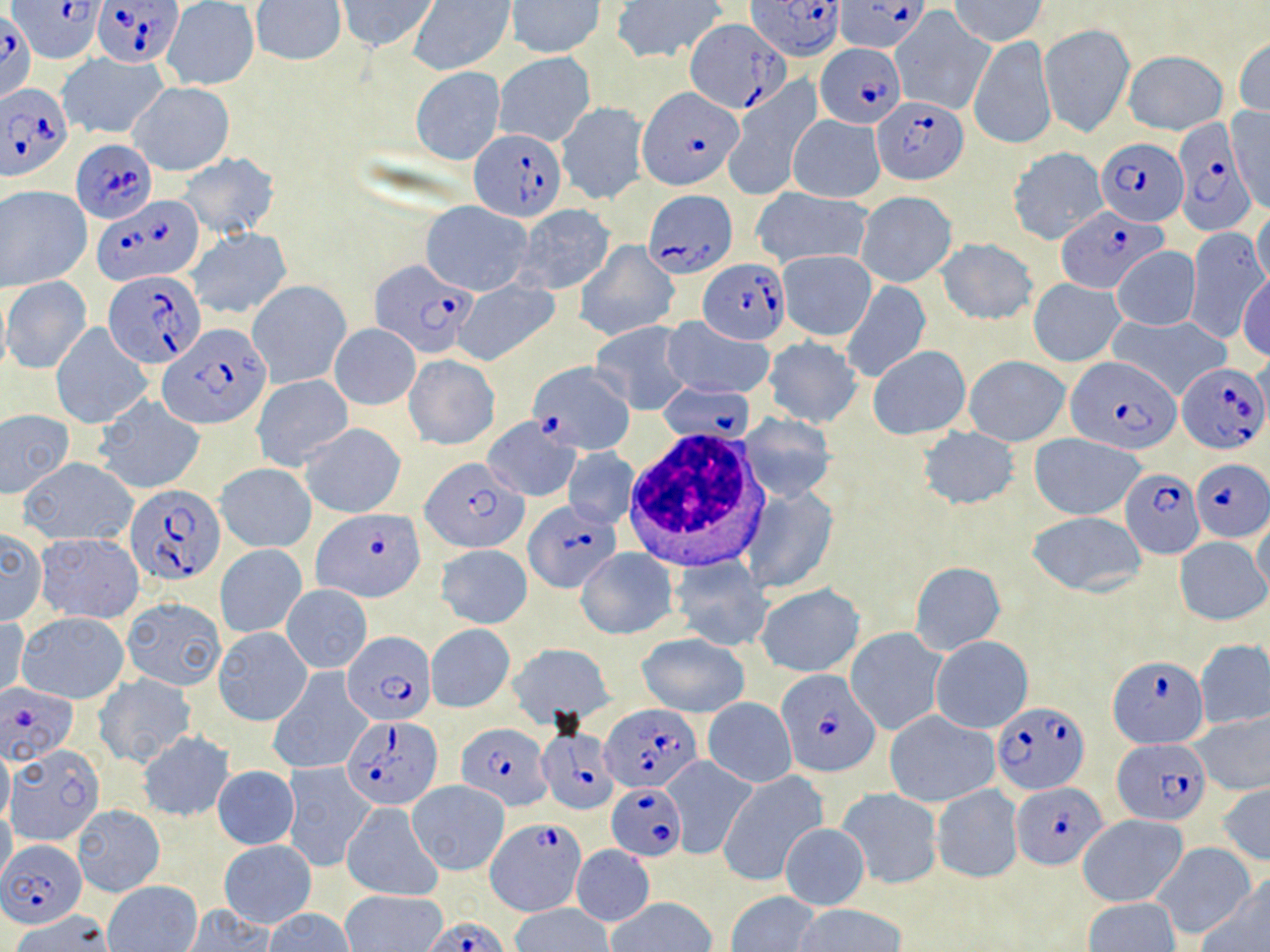
{
  "slide_level_diagnosis": "Plasmodium falciparum",
  "preparation": "thin blood film",
  "image_size": "1270×952 pixels",
  "plasmodium_falciparum_infected_red_blood_cell_locations": "approximate bounding boxes as named x1/y1/x2/y2 corners in pixels: (x1=14, y1=0, x2=104, y2=65), (x1=93, y1=0, x2=183, y2=68), (x1=747, y1=0, x2=843, y2=60), (x1=836, y1=2, x2=929, y2=53), (x1=0, y1=10, x2=36, y2=102), (x1=684, y1=19, x2=786, y2=116), (x1=815, y1=44, x2=905, y2=128), (x1=0, y1=85, x2=73, y2=183), (x1=637, y1=86, x2=746, y2=192), (x1=871, y1=96, x2=969, y2=184), (x1=1173, y1=124, x2=1249, y2=240), (x1=469, y1=131, x2=566, y2=222), (x1=1096, y1=137, x2=1188, y2=225), (x1=71, y1=138, x2=157, y2=223), (x1=645, y1=190, x2=735, y2=278), (x1=93, y1=196, x2=203, y2=285), (x1=1056, y1=206, x2=1166, y2=293), (x1=700, y1=260, x2=791, y2=343), (x1=370, y1=261, x2=477, y2=358), (x1=102, y1=271, x2=207, y2=368), (x1=160, y1=323, x2=272, y2=428), (x1=1067, y1=357, x2=1180, y2=454), (x1=528, y1=360, x2=634, y2=455), (x1=1177, y1=362, x2=1267, y2=453), (x1=656, y1=381, x2=755, y2=442), (x1=420, y1=455, x2=526, y2=554), (x1=1191, y1=459, x2=1268, y2=540), (x1=1121, y1=468, x2=1204, y2=559), (x1=126, y1=484, x2=225, y2=585), (x1=526, y1=501, x2=619, y2=592), (x1=316, y1=509, x2=423, y2=603), (x1=342, y1=632, x2=436, y2=727), (x1=1108, y1=654, x2=1208, y2=748), (x1=775, y1=671, x2=881, y2=778), (x1=0, y1=685, x2=80, y2=769), (x1=993, y1=700, x2=1089, y2=794), (x1=601, y1=705, x2=700, y2=792), (x1=341, y1=713, x2=444, y2=809), (x1=456, y1=722, x2=552, y2=809), (x1=537, y1=728, x2=620, y2=816), (x1=1113, y1=738, x2=1212, y2=825), (x1=606, y1=782, x2=685, y2=862), (x1=1013, y1=782, x2=1104, y2=867), (x1=487, y1=817, x2=584, y2=913), (x1=0, y1=839, x2=88, y2=929), (x1=422, y1=917, x2=512, y2=952)",
  "uninfected_red_blood_cell_locations": "approximate bounding boxes as named x1/y1/x2/y2 corners in pixels: (x1=337, y1=0, x2=439, y2=53), (x1=952, y1=0, x2=1046, y2=44), (x1=252, y1=1, x2=346, y2=66), (x1=409, y1=1, x2=515, y2=74), (x1=507, y1=1, x2=606, y2=58), (x1=611, y1=1, x2=722, y2=63), (x1=163, y1=2, x2=260, y2=90), (x1=892, y1=9, x2=994, y2=115), (x1=1040, y1=23, x2=1134, y2=137), (x1=1234, y1=35, x2=1270, y2=120), (x1=968, y1=37, x2=1056, y2=150), (x1=1124, y1=51, x2=1227, y2=135), (x1=57, y1=52, x2=170, y2=138), (x1=494, y1=52, x2=595, y2=146), (x1=411, y1=67, x2=505, y2=165), (x1=128, y1=82, x2=236, y2=175), (x1=723, y1=86, x2=818, y2=199), (x1=555, y1=101, x2=649, y2=205), (x1=1228, y1=107, x2=1269, y2=214), (x1=788, y1=116, x2=885, y2=201), (x1=1007, y1=147, x2=1108, y2=245), (x1=178, y1=151, x2=281, y2=239), (x1=1, y1=185, x2=92, y2=290), (x1=752, y1=188, x2=873, y2=269), (x1=856, y1=192, x2=956, y2=288), (x1=421, y1=201, x2=532, y2=295), (x1=514, y1=204, x2=617, y2=296), (x1=1252, y1=210, x2=1270, y2=293), (x1=1183, y1=227, x2=1266, y2=343), (x1=188, y1=228, x2=292, y2=321), (x1=936, y1=237, x2=1037, y2=327), (x1=574, y1=241, x2=679, y2=341), (x1=1111, y1=247, x2=1201, y2=330), (x1=776, y1=250, x2=877, y2=341), (x1=1237, y1=273, x2=1270, y2=362), (x1=2, y1=276, x2=92, y2=374), (x1=452, y1=278, x2=560, y2=366), (x1=1028, y1=278, x2=1125, y2=366), (x1=248, y1=280, x2=351, y2=389), (x1=840, y1=280, x2=930, y2=383), (x1=0, y1=284, x2=11, y2=380), (x1=1104, y1=314, x2=1231, y2=401), (x1=662, y1=318, x2=777, y2=400), (x1=590, y1=322, x2=691, y2=415), (x1=51, y1=323, x2=151, y2=429), (x1=328, y1=323, x2=420, y2=410), (x1=763, y1=337, x2=862, y2=427), (x1=867, y1=345, x2=970, y2=439), (x1=403, y1=354, x2=499, y2=450), (x1=965, y1=356, x2=1070, y2=446), (x1=251, y1=374, x2=354, y2=470), (x1=93, y1=394, x2=207, y2=494), (x1=0, y1=408, x2=74, y2=497), (x1=738, y1=414, x2=836, y2=501), (x1=483, y1=417, x2=581, y2=502), (x1=301, y1=422, x2=406, y2=518), (x1=918, y1=427, x2=1020, y2=509), (x1=1029, y1=434, x2=1147, y2=519), (x1=564, y1=448, x2=638, y2=529), (x1=17, y1=457, x2=138, y2=547), (x1=216, y1=463, x2=316, y2=551), (x1=742, y1=487, x2=838, y2=593), (x1=1027, y1=511, x2=1147, y2=597), (x1=1250, y1=517, x2=1270, y2=608), (x1=0, y1=529, x2=48, y2=627), (x1=34, y1=532, x2=144, y2=624), (x1=1174, y1=536, x2=1269, y2=627), (x1=215, y1=544, x2=306, y2=638), (x1=436, y1=544, x2=533, y2=629), (x1=576, y1=547, x2=678, y2=639), (x1=668, y1=557, x2=773, y2=650), (x1=910, y1=561, x2=1005, y2=655), (x1=282, y1=585, x2=372, y2=673), (x1=755, y1=585, x2=865, y2=677), (x1=121, y1=596, x2=227, y2=690), (x1=17, y1=611, x2=129, y2=704), (x1=0, y1=615, x2=30, y2=702), (x1=425, y1=624, x2=514, y2=713), (x1=213, y1=626, x2=312, y2=726), (x1=846, y1=628, x2=947, y2=736), (x1=635, y1=633, x2=749, y2=717), (x1=930, y1=636, x2=1033, y2=734), (x1=1195, y1=639, x2=1270, y2=730), (x1=507, y1=643, x2=614, y2=725), (x1=269, y1=669, x2=372, y2=775), (x1=95, y1=673, x2=196, y2=769), (x1=703, y1=698, x2=797, y2=787), (x1=1189, y1=709, x2=1269, y2=796), (x1=884, y1=710, x2=1000, y2=807), (x1=137, y1=731, x2=235, y2=822), (x1=0, y1=745, x2=13, y2=827), (x1=8, y1=747, x2=105, y2=846), (x1=661, y1=756, x2=755, y2=859), (x1=281, y1=763, x2=375, y2=870), (x1=213, y1=766, x2=298, y2=849), (x1=717, y1=772, x2=828, y2=885), (x1=408, y1=780, x2=509, y2=874), (x1=931, y1=783, x2=1024, y2=883), (x1=1217, y1=784, x2=1270, y2=865), (x1=835, y1=787, x2=944, y2=891), (x1=72, y1=803, x2=165, y2=896), (x1=341, y1=803, x2=441, y2=901), (x1=0, y1=807, x2=17, y2=886), (x1=1076, y1=814, x2=1190, y2=907), (x1=779, y1=824, x2=870, y2=911), (x1=220, y1=840, x2=315, y2=928), (x1=1149, y1=843, x2=1256, y2=940), (x1=571, y1=845, x2=654, y2=926), (x1=1203, y1=872, x2=1270, y2=952), (x1=104, y1=882, x2=202, y2=951), (x1=342, y1=890, x2=449, y2=952), (x1=727, y1=891, x2=822, y2=952), (x1=608, y1=897, x2=716, y2=952), (x1=1083, y1=898, x2=1181, y2=952), (x1=510, y1=903, x2=614, y2=952), (x1=793, y1=903, x2=906, y2=952), (x1=179, y1=905, x2=275, y2=951), (x1=264, y1=908, x2=354, y2=952), (x1=11, y1=911, x2=115, y2=952)",
  "white_blood_cell_locations": "approximate bounding boxes as named x1/y1/x2/y2 corners in pixels: (x1=625, y1=429, x2=772, y2=573)",
  "magnification": "1000x",
  "modality": "optical microscopy",
  "stain": "May-Grünwald-Giemsa",
  "field_of_view": "single"
}